State which cell type is depicted.
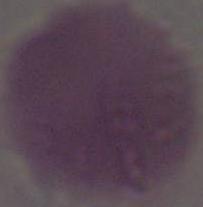
An erythrocyte.

modality = micrograph
magnification = 1000x